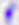

identification = Toxoplasma gondii
modality = photomicrograph
magnification = 400x